Find each parasitized red blood cell.
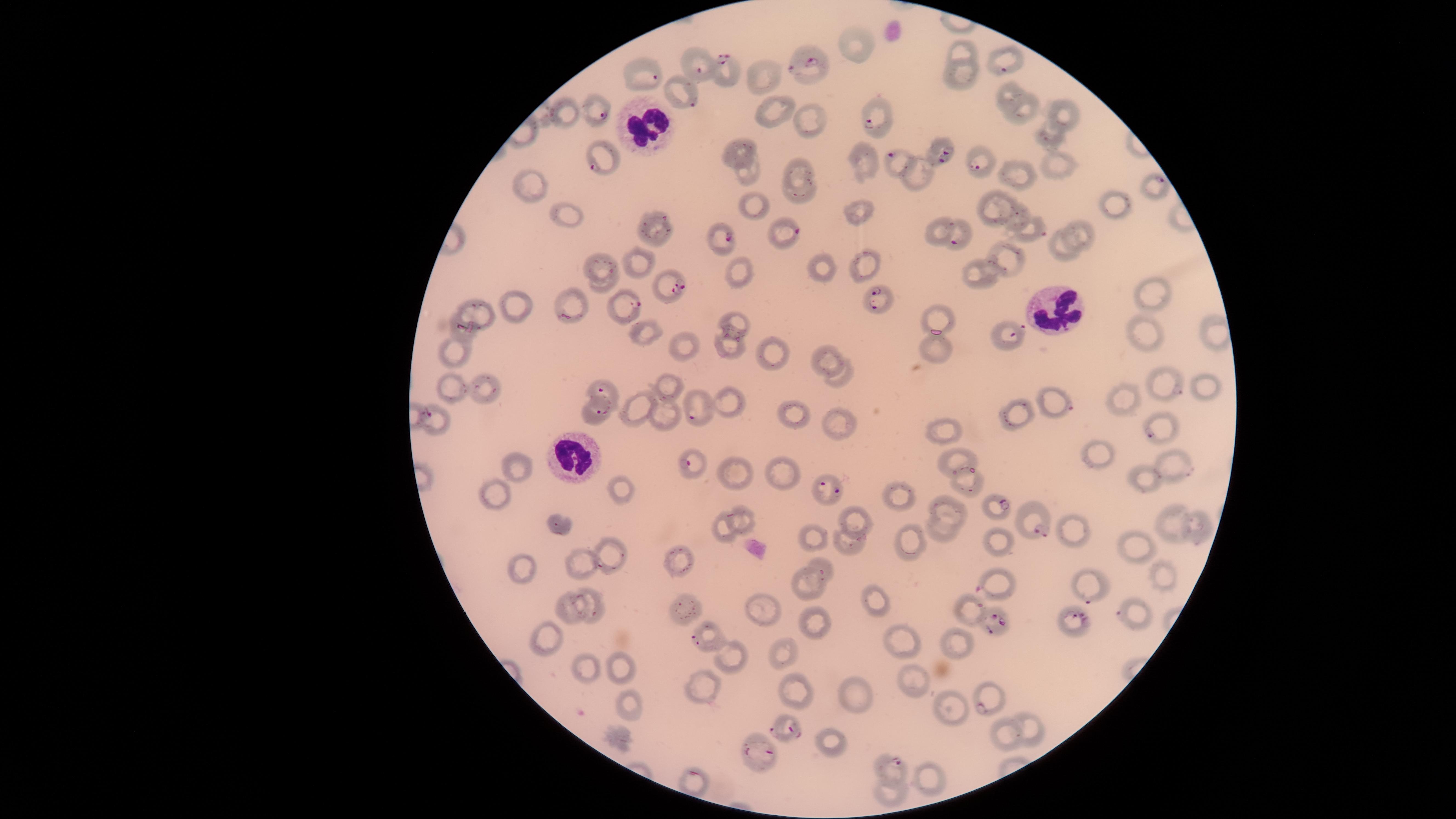

Approximate marker points, in pixels from the top-left corner.
Parasitized red blood cells: (x=727, y=62), (x=811, y=62), (x=1002, y=71), (x=701, y=72), (x=654, y=76), (x=689, y=98), (x=602, y=112), (x=870, y=122), (x=1046, y=139), (x=944, y=155), (x=893, y=157), (x=979, y=166), (x=594, y=169), (x=1159, y=183), (x=791, y=230), (x=1041, y=231), (x=727, y=238), (x=957, y=242), (x=678, y=289), (x=874, y=295), (x=631, y=304), (x=1017, y=332), (x=1172, y=388), (x=599, y=391), (x=1060, y=406), (x=601, y=413), (x=695, y=417), (x=1155, y=435), (x=687, y=462), (x=837, y=492), (x=1001, y=506), (x=1034, y=525), (x=980, y=588), (x=1086, y=595), (x=977, y=606), (x=1081, y=620), (x=1000, y=626), (x=697, y=640), (x=984, y=707), (x=790, y=730), (x=770, y=753), (x=899, y=765).

{
  "species": "Plasmodium falciparum",
  "field_of_view": "single",
  "stain": "Giemsa",
  "capture": "smartphone photograph through the microscope eyepiece",
  "uninfected_red_blood_cells": "approximate marker points, in pixels from the top-left corner: (x=861, y=35), (x=960, y=49), (x=767, y=75), (x=960, y=76), (x=1006, y=93), (x=770, y=110), (x=1021, y=111), (x=1068, y=114), (x=570, y=115), (x=812, y=126), (x=747, y=151), (x=864, y=156), (x=801, y=169), (x=1062, y=169), (x=750, y=175), (x=920, y=175), (x=1018, y=181), (x=530, y=189), (x=801, y=193), (x=753, y=201), (x=1002, y=201), (x=1119, y=202), (x=861, y=215), (x=1019, y=216), (x=566, y=220), (x=939, y=225), (x=656, y=227), (x=1085, y=234), (x=1064, y=251), (x=606, y=262), (x=1012, y=263), (x=641, y=265), (x=868, y=266), (x=821, y=268), (x=741, y=272), (x=979, y=276), (x=603, y=284), (x=1163, y=298), (x=573, y=299), (x=520, y=309), (x=482, y=310), (x=942, y=315), (x=737, y=320), (x=1145, y=331), (x=466, y=334), (x=650, y=334), (x=685, y=344), (x=733, y=349), (x=457, y=351), (x=821, y=352), (x=934, y=352), (x=770, y=355), (x=839, y=378), (x=488, y=389), (x=674, y=389), (x=1210, y=389), (x=454, y=390), (x=1125, y=394), (x=735, y=406), (x=1009, y=407), (x=643, y=410), (x=799, y=412), (x=662, y=416), (x=440, y=420), (x=839, y=420), (x=944, y=429), (x=956, y=457), (x=1100, y=458), (x=1170, y=464), (x=515, y=468), (x=781, y=472), (x=740, y=478), (x=1143, y=483), (x=969, y=486), (x=622, y=491), (x=496, y=494), (x=898, y=496), (x=946, y=508), (x=858, y=519), (x=743, y=521), (x=1199, y=522), (x=1170, y=523), (x=558, y=525), (x=939, y=531), (x=721, y=533), (x=1073, y=533), (x=817, y=541), (x=848, y=543), (x=911, y=543), (x=998, y=543), (x=1140, y=543), (x=613, y=555), (x=579, y=559), (x=524, y=566), (x=682, y=567), (x=824, y=574), (x=1165, y=578), (x=806, y=589), (x=877, y=598), (x=592, y=604), (x=685, y=608), (x=1141, y=609), (x=759, y=610), (x=575, y=612), (x=813, y=629), (x=547, y=636), (x=960, y=646), (x=905, y=647), (x=783, y=653), (x=733, y=660), (x=623, y=666), (x=586, y=667), (x=914, y=682), (x=708, y=685), (x=851, y=694), (x=796, y=696), (x=628, y=704), (x=958, y=708), (x=1031, y=727), (x=1005, y=735), (x=831, y=740), (x=928, y=777), (x=890, y=794)",
  "image_size": "1456×819 pixels",
  "preparation": "thin blood film",
  "white_blood_cells": "approximate marker points, in pixels from the top-left corner: (x=642, y=125), (x=1055, y=311), (x=572, y=457)",
  "visible_region": "circular"
}